Locate every Plasmodium parasite.
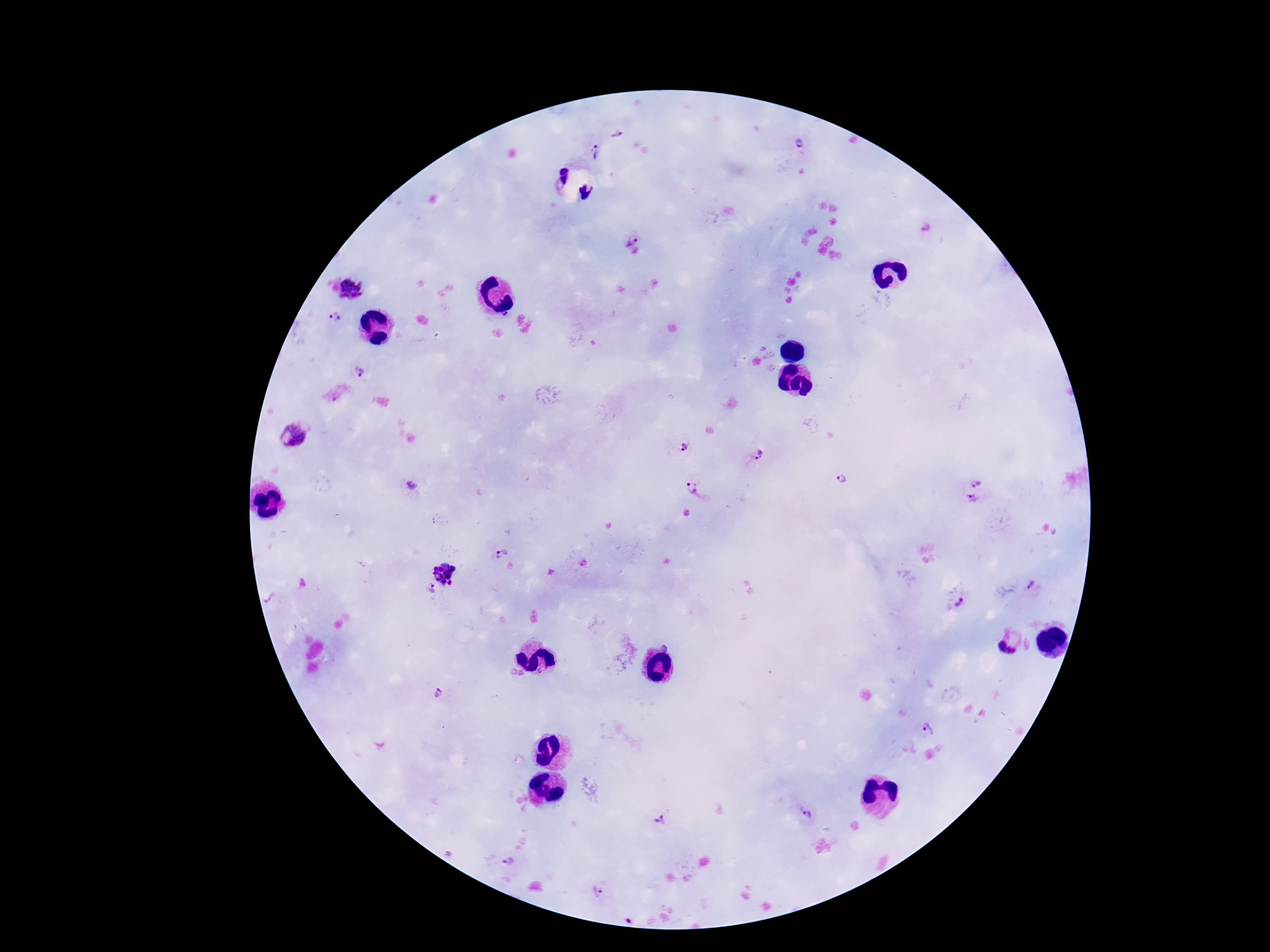

Approximate centers as [x, y] in pixels.
Plasmodium parasites: [616, 134], [799, 145], [596, 153], [926, 229], [630, 239], [352, 288], [507, 315], [334, 317], [359, 372], [293, 435], [684, 446], [758, 456], [841, 480], [977, 480], [413, 485], [692, 487], [973, 500], [501, 553], [446, 572], [1032, 584], [431, 590], [960, 602], [1009, 644], [666, 647], [438, 695], [929, 729], [806, 817], [661, 822], [509, 861], [597, 892].

Smartphone photograph taken through the microscope eyepiece. Thick blood film. Giemsa stain. 100x magnification. Image is 1270×952 pixels. Single field of view. Patient malaria status: positive.